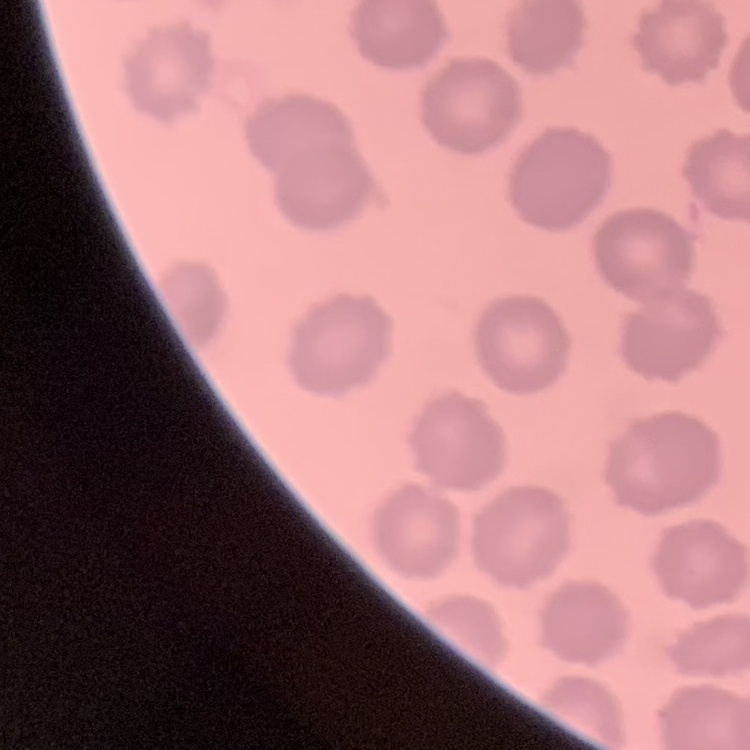

Summary:
  - Red blood cell morphology: no rouleaux formation
  - Preparation: thin blood film
  - Stain: Field's or Giemsa
  - Image type: one tile cut from a larger photomicrograph